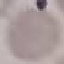 Result: negative for malaria parasites. Giemsa stain. Thin blood smear. Photographed with a smartphone camera at the microscope eyepiece. Automatically extracted cell patch, resized to 64 × 64 pixels.